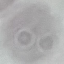
Malaria status: uninfected. Automatically extracted cell patch, resized to 64 × 64 pixels. Thin blood film. Photographed with a smartphone camera at the microscope eyepiece. Giemsa-stained preparation.